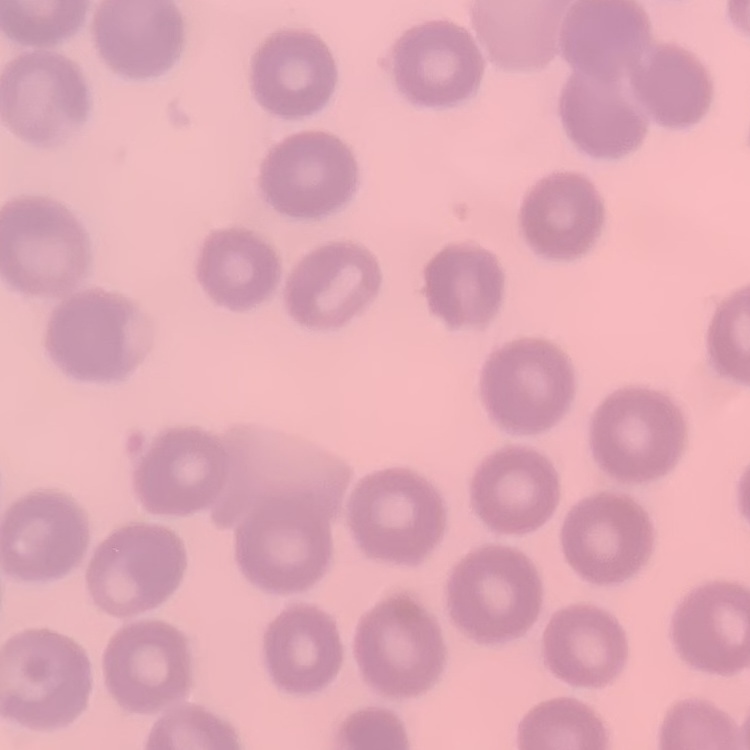

Summary:
  - Red blood cell morphology: no rouleaux formation
  - Image type: one tile cut from a larger photomicrograph
  - Stain: Field's or Giemsa
  - Preparation: thin blood smear